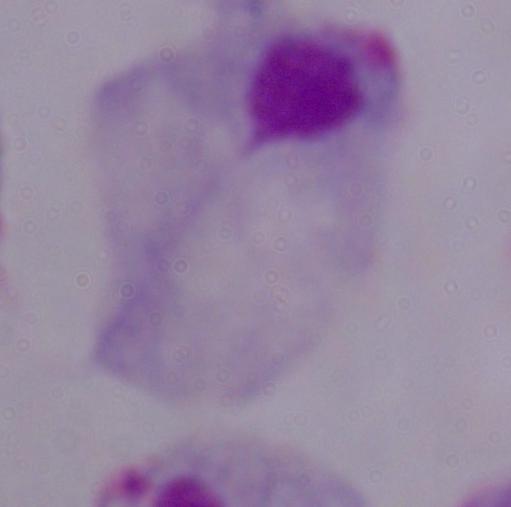
Summary:
  - Identification: trichomonad
  - Magnification: 1000x
  - Modality: photomicrograph